Locate and identify every blood parasite.
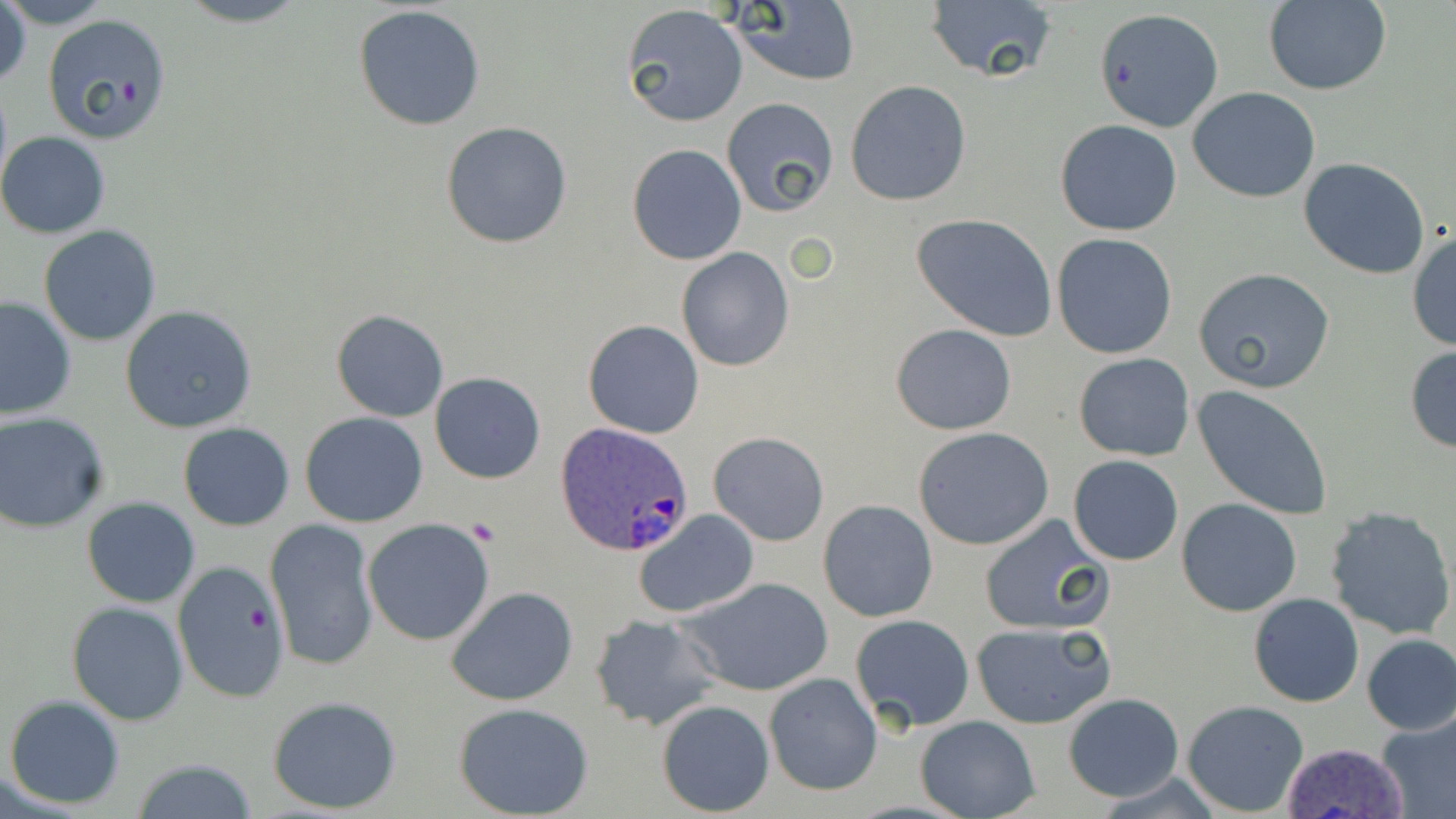

Approximate bounding boxes as (x1, y1, x2, y2) in pixels.
Plasmodium ovale-infected red blood cells: (556, 424, 695, 557), (1277, 740, 1410, 819).
No Plasmodium falciparum, Plasmodium malariae, Plasmodium vivax, Babesia divergens, or Trypanosoma brucei observed.

Uninfected red blood cell locations: (0, 0, 31, 92), (1, 0, 116, 28), (171, 0, 317, 27), (723, 1, 860, 86), (922, 1, 1061, 85), (1261, 1, 1391, 94), (353, 5, 487, 132), (620, 5, 747, 128), (1094, 6, 1224, 134), (43, 16, 173, 148), (845, 80, 971, 206), (1188, 88, 1321, 202), (722, 97, 839, 216), (1055, 119, 1184, 236), (440, 121, 572, 249), (0, 132, 110, 238), (627, 144, 746, 265), (1300, 158, 1431, 279), (912, 213, 1057, 342), (39, 225, 162, 347), (1407, 230, 1456, 350), (1051, 234, 1178, 359), (676, 247, 793, 371), (1192, 268, 1335, 394), (0, 297, 75, 420), (121, 306, 258, 433), (330, 309, 449, 423), (583, 320, 705, 439), (890, 322, 1017, 435), (1404, 345, 1456, 452), (1072, 352, 1195, 461), (429, 373, 546, 484), (1191, 384, 1334, 521), (301, 411, 428, 527), (0, 412, 114, 534), (178, 422, 295, 531), (913, 427, 1054, 550), (708, 430, 830, 546), (1067, 455, 1184, 566), (82, 498, 199, 606), (1177, 498, 1302, 616), (818, 499, 938, 622), (1326, 507, 1456, 639), (632, 510, 760, 619), (977, 514, 1114, 637), (266, 518, 378, 673), (363, 518, 496, 646), (176, 562, 289, 704), (680, 575, 835, 696), (446, 585, 579, 707), (1248, 593, 1364, 708), (67, 601, 189, 724), (588, 613, 723, 730), (850, 614, 975, 732), (971, 621, 1117, 729), (1360, 635, 1456, 735), (764, 672, 881, 795), (1061, 693, 1184, 803), (5, 694, 125, 808), (267, 695, 402, 814), (655, 699, 775, 816), (1182, 700, 1310, 816), (454, 702, 594, 818), (1375, 709, 1456, 819), (915, 715, 1039, 819), (129, 759, 263, 817). Platelet locations: (468, 519, 500, 545). Slide-level diagnosis: Plasmodium ovale. Captured at 1000x magnification. May-Grünwald-Giemsa-stained preparation. One field of a larger specimen. Thin blood smear. Optical microscopy. Image is 1456×819 pixels.